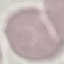

Malaria status: uninfected. Thin smear of blood. Automatically extracted cell patch, resized to 64 × 64 pixels. Photographed with a smartphone camera at the microscope eyepiece. Giemsa-stained preparation.